Give the extent of all Plasmodium ovale-infected red blood cells.
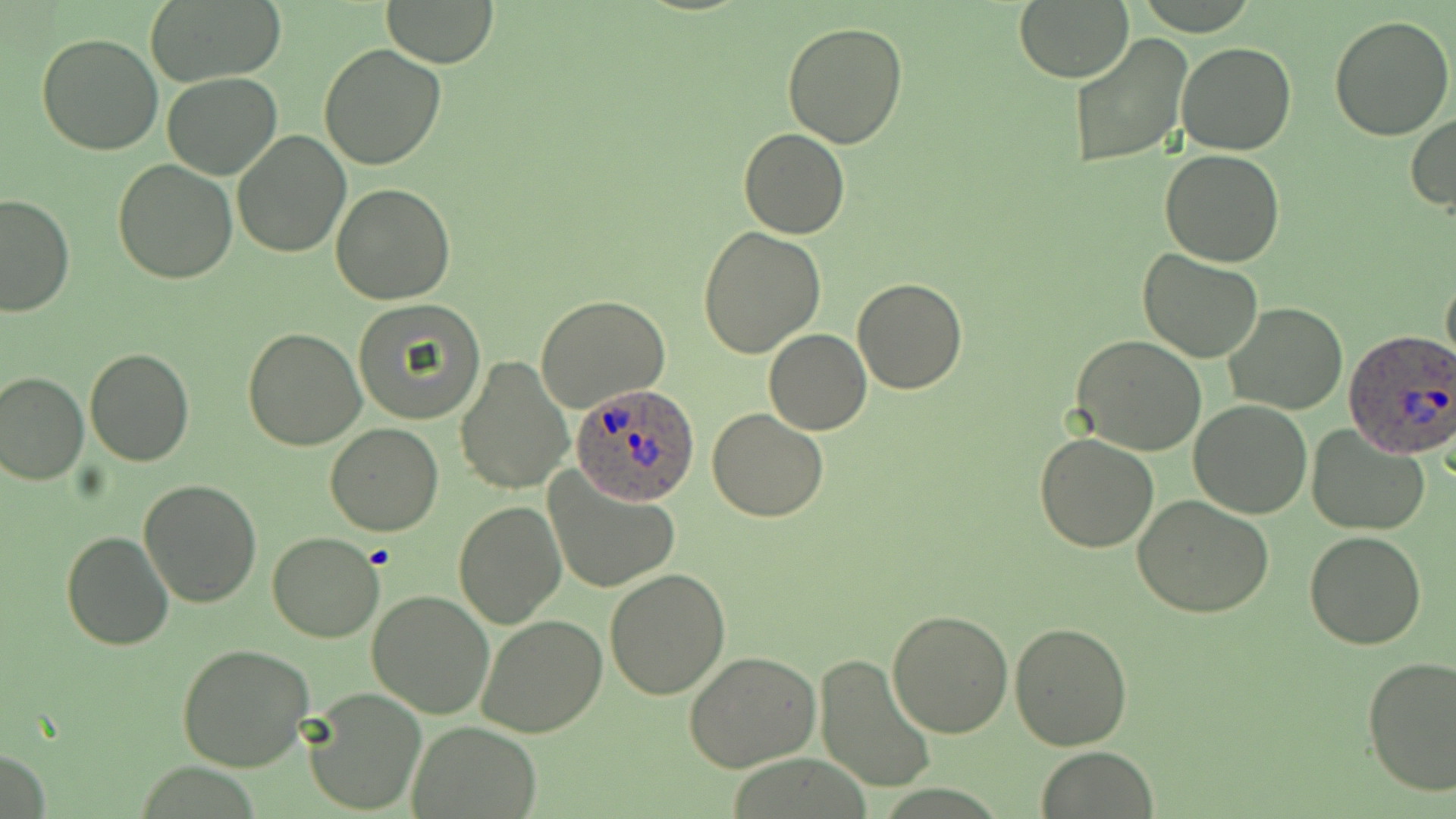
Approximate bounding boxes as (x1, y1, x2, y2) in pixels.
Plasmodium ovale-infected red blood cells: (1345, 330, 1456, 460), (570, 382, 703, 507).

Summary:
  - Uninfected red blood cell locations: (143, 0, 285, 86), (1013, 0, 1134, 83), (380, 1, 501, 66), (1329, 13, 1455, 140), (782, 22, 910, 149), (36, 32, 166, 156), (1067, 32, 1193, 169), (1175, 41, 1296, 157), (319, 43, 447, 170), (163, 73, 283, 180), (1406, 112, 1456, 214), (739, 127, 849, 239), (231, 129, 351, 259), (1159, 148, 1285, 267), (112, 158, 238, 284), (331, 181, 456, 303), (0, 193, 77, 316), (697, 227, 825, 360), (1137, 250, 1264, 364), (1441, 268, 1456, 373), (853, 278, 967, 393), (535, 294, 671, 413), (353, 300, 486, 424), (1223, 303, 1350, 416), (243, 326, 366, 449), (764, 329, 871, 435), (1071, 336, 1207, 457), (84, 346, 194, 466), (455, 356, 574, 496), (0, 369, 89, 485), (1189, 399, 1312, 519), (707, 408, 828, 522), (324, 422, 444, 536), (1306, 425, 1430, 536), (1034, 432, 1161, 552), (542, 470, 680, 595), (139, 479, 264, 607), (1133, 493, 1275, 618), (453, 500, 565, 629), (61, 530, 174, 651), (1303, 531, 1426, 649), (266, 532, 384, 642), (605, 569, 731, 700), (366, 590, 495, 718), (886, 608, 1015, 738), (475, 614, 606, 739), (1009, 623, 1134, 749), (177, 643, 313, 772), (684, 651, 824, 771), (813, 653, 938, 795), (1360, 655, 1456, 796), (302, 687, 428, 816), (409, 721, 540, 815), (1034, 747, 1159, 818)
  - Slide-level diagnosis: Plasmodium ovale
  - Field of view: single
  - Magnification: 1000x
  - Modality: light microscopy
  - Stain: May-Grünwald-Giemsa
  - Preparation: thin blood smear
  - Image size: 1456×819 pixels